Locate every uninfected red blood cell.
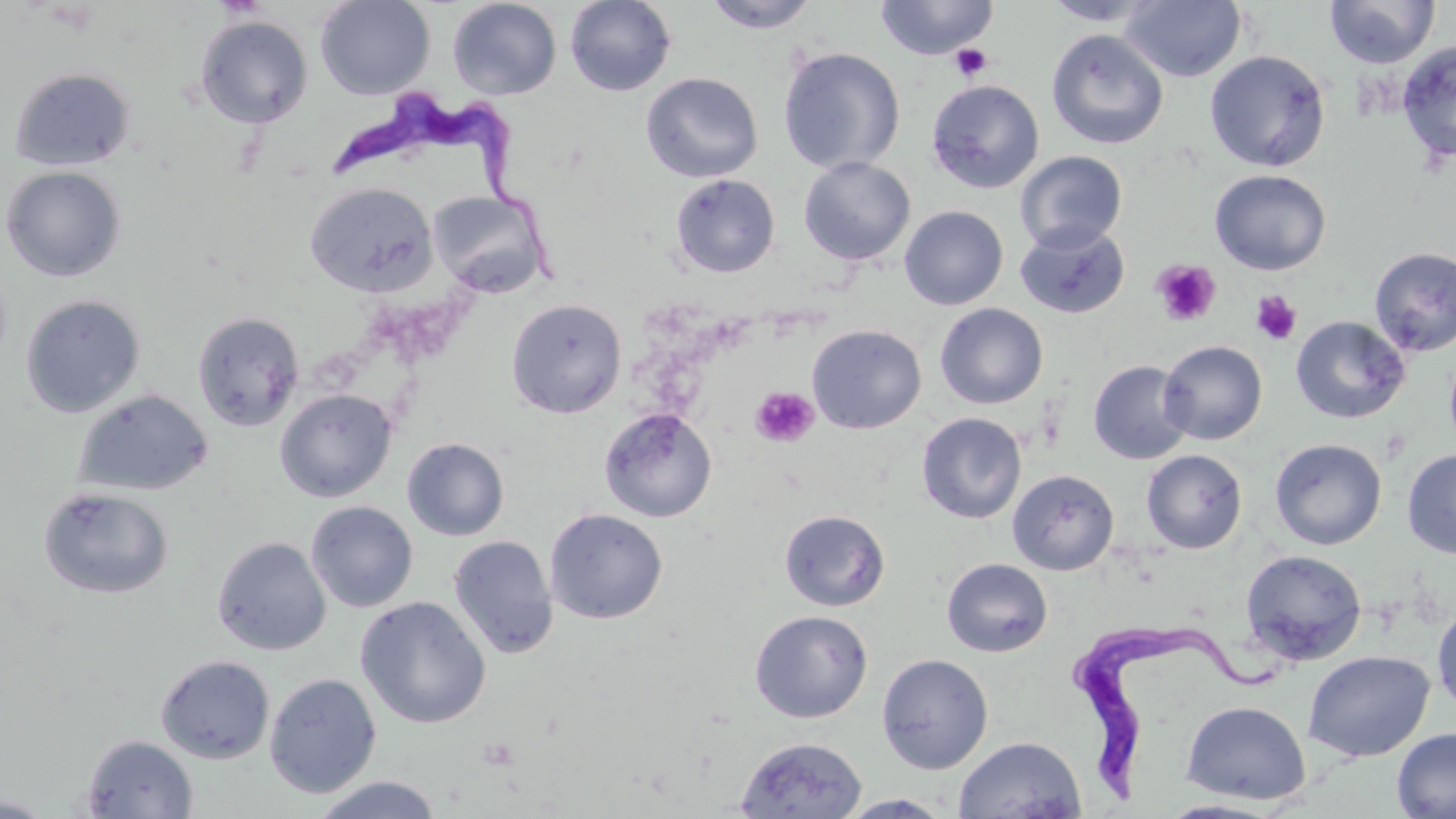

Approximate bounding boxes as (x1,y1)-(x2,y2) corner pairs in pixels.
Uninfected red blood cells: (316,0)-(434,100), (448,0)-(562,100), (565,0)-(677,96), (874,0)-(999,60), (1042,0)-(1160,26), (1120,0)-(1246,82), (1324,0)-(1440,69), (701,1)-(824,33), (195,15)-(313,128), (1046,29)-(1168,149), (1396,40)-(1456,165), (778,47)-(905,175), (1205,49)-(1331,172), (9,66)-(136,172), (640,72)-(763,182), (926,79)-(1044,193), (1015,151)-(1127,253), (799,156)-(916,266), (1,166)-(126,282), (1209,169)-(1331,275), (670,173)-(780,277), (305,182)-(438,296), (427,190)-(551,298), (899,206)-(1008,310), (1015,223)-(1130,319), (1369,246)-(1456,356), (20,295)-(145,417), (506,298)-(628,418), (935,303)-(1048,409), (192,312)-(304,431), (1290,315)-(1411,424), (807,324)-(926,434), (1158,340)-(1268,445), (1444,346)-(1456,456), (1088,360)-(1193,464), (275,389)-(397,503), (74,390)-(213,496), (599,407)-(717,522), (916,412)-(1027,523), (402,437)-(509,541), (1269,438)-(1387,550), (1402,448)-(1456,558), (1141,450)-(1247,553), (1007,469)-(1119,576), (38,486)-(174,599), (306,501)-(418,613), (544,508)-(668,624), (779,509)-(890,611), (448,535)-(559,659), (211,536)-(331,655), (1240,549)-(1367,666), (941,558)-(1053,657), (355,596)-(491,728), (1431,603)-(1456,713), (750,610)-(873,723), (1303,650)-(1436,762), (876,653)-(994,774), (156,654)-(274,764), (264,673)-(382,798), (1180,700)-(1311,804), (1392,727)-(1456,819), (81,734)-(198,818), (953,735)-(1087,819), (735,736)-(868,818), (310,775)-(443,818), (838,793)-(953,818), (0,794)-(56,817), (1157,800)-(1283,818).

slide-level diagnosis = Trypanosoma brucei
preparation = thin blood smear
Trypanosoma brucei locations = approximate bounding boxes as (x1,y1)-(x2,y2) corner pairs in pixels: (328,85)-(560,283), (1071,625)-(1286,809)
field of view = single
stain = May-Grünwald-Giemsa
image size = 1456×819 pixels
magnification = 1000x
modality = optical microscopy
platelet locations = approximate bounding boxes as (x1,y1)-(x2,y2) corner pairs in pixels: (949,43)-(994,81), (1151,259)-(1221,327), (1251,290)-(1303,346), (750,386)-(819,448), (1380,427)-(1412,463), (477,736)-(521,772)